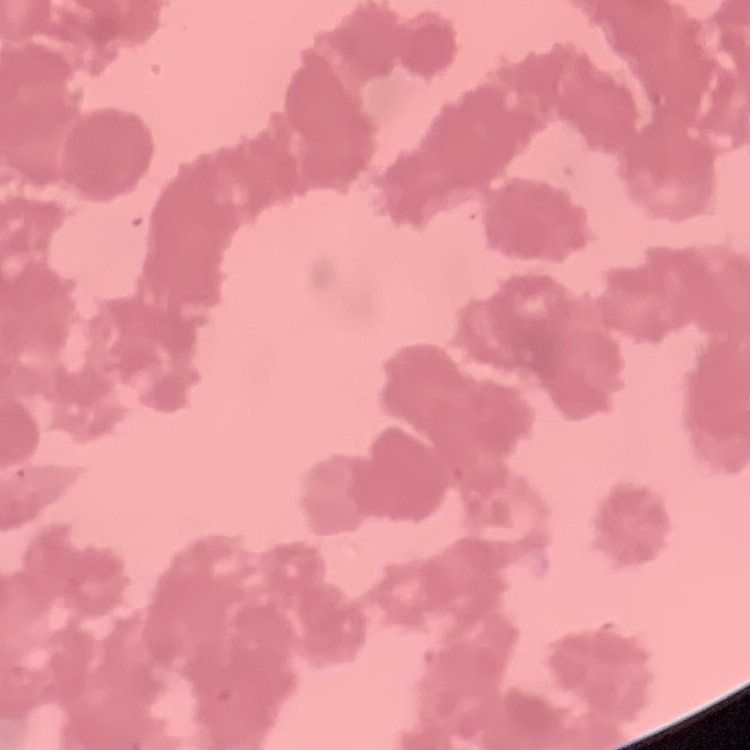
The erythrocytes show rouleaux formation. Field's or Giemsa stain. One tile cut from a larger photomicrograph. Thin peripheral smear.